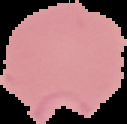

Summary:
  - Image size: 127×124 pixels
  - Image type: segmented cell region on a black background
  - Preparation: thin blood film
  - Malaria status: parasitized